Report the malaria status of this cell.
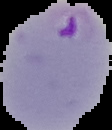
It is parasitized.

Summary:
  - Image type: segmented cell region with the area outside set to black
  - Image size: 112×130 pixels
  - Preparation: thin blood film